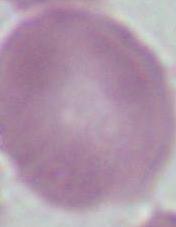

Summary:
  - Modality: photomicrograph
  - Magnification: 1000x
  - Identification: erythrocyte